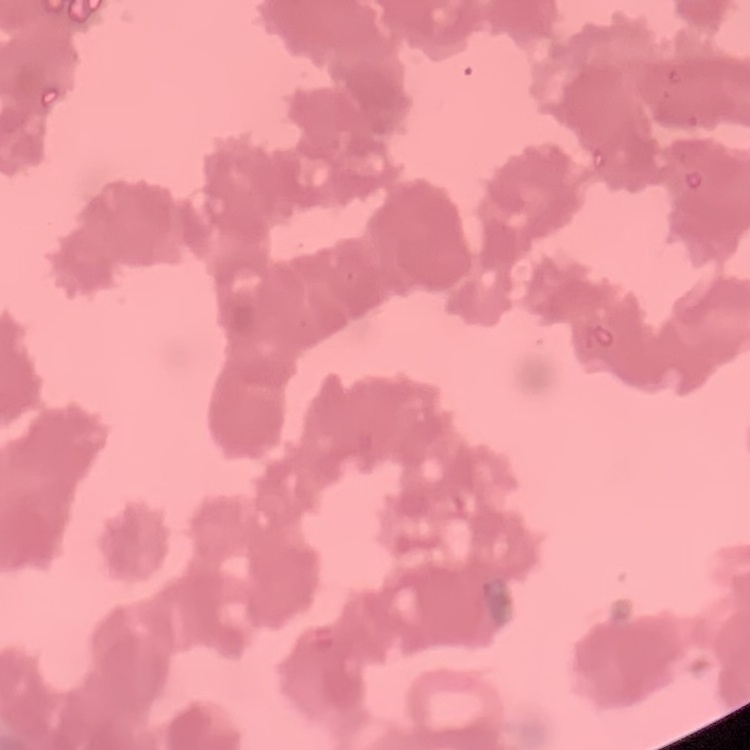

Summary:
  - Red blood cell morphology: rouleaux formation
  - Preparation: thin peripheral smear
  - Stain: Field's or Giemsa
  - Image type: square crop of a larger photomicrograph